Assess this cell for malaria.
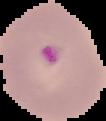
Parasitized.

Segmented cell region on a black background. From a thin blood smear. Image is 106×121 pixels.